Point out each malaria parasite.
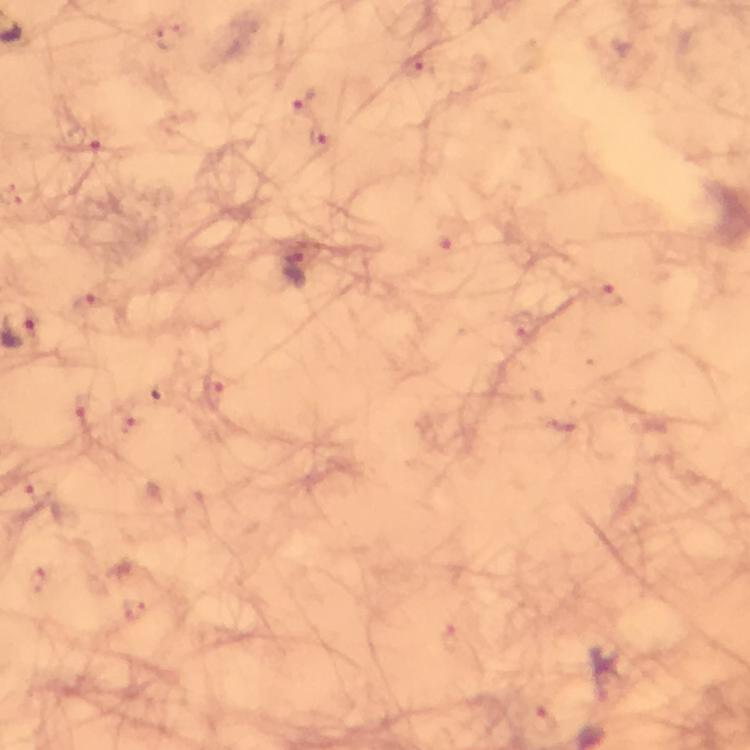
Approximate centers as {x, y} in pixels.
Malaria parasites: {295, 269}.

Summary:
  - Image size: 750×750 pixels
  - Magnification: 100x
  - Immersion oil: used
  - Cropped from: a single field of view
  - Preparation: thick smear
  - Context: from a diagnostic examination for malaria
  - Stain: Giemsa
  - Capture: smartphone mounted on the microscope